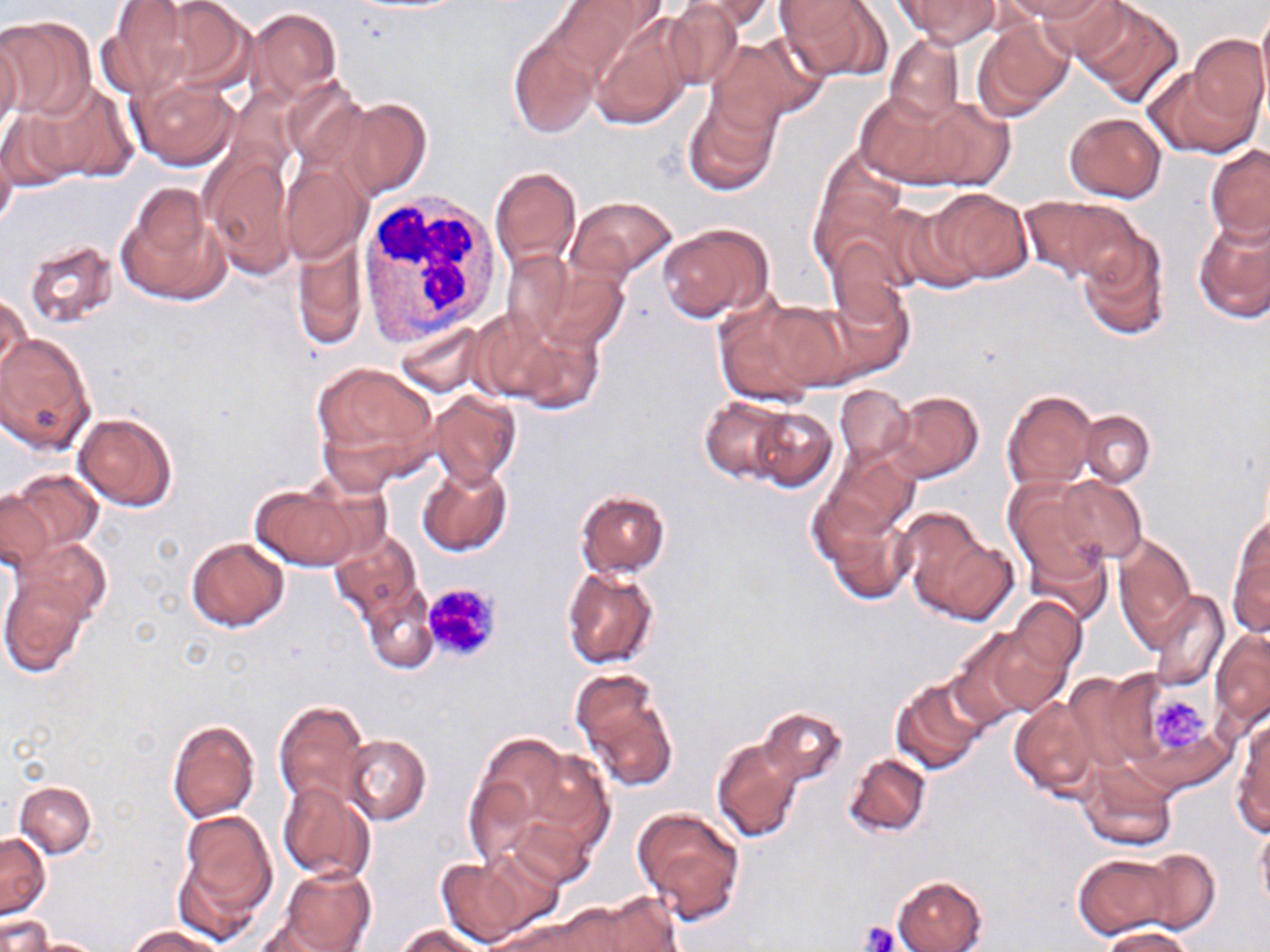
{
  "slide_level_diagnosis": "negative for blood parasites",
  "magnification": "1000x",
  "modality": "optical microscopy",
  "white_blood_cell_locations": "approximate bounding boxes as (x1, y1, x2, y2) in pixels: (358, 192, 506, 345)",
  "platelet_locations": "approximate bounding boxes as (x1, y1, x2, y2) in pixels: (422, 582, 501, 662), (1148, 690, 1212, 755), (860, 922, 900, 952)",
  "field_of_view": "one of a larger specimen",
  "image_size": "1270×952 pixels",
  "preparation": "thin blood film",
  "stain": "May-Grünwald-Giemsa",
  "uninfected_red_blood_cell_locations": "approximate bounding boxes as (x1, y1, x2, y2) in pixels: (154, 0, 259, 94), (550, 0, 658, 79), (680, 0, 777, 32), (776, 0, 888, 82), (894, 0, 1000, 46), (999, 0, 1112, 22), (1038, 0, 1135, 71), (100, 1, 195, 99), (661, 2, 744, 91), (1076, 2, 1183, 106), (1256, 2, 1270, 108), (247, 5, 342, 102), (0, 15, 96, 120), (589, 15, 694, 130), (972, 16, 1073, 121), (508, 30, 599, 137), (0, 31, 22, 143), (709, 33, 826, 130), (1188, 33, 1270, 136), (884, 35, 964, 124), (1143, 62, 1259, 158), (128, 77, 238, 169), (281, 79, 366, 168), (27, 83, 136, 182), (855, 89, 980, 188), (683, 94, 781, 196), (906, 95, 1016, 193), (3, 98, 93, 189), (342, 98, 431, 198), (1064, 113, 1167, 202), (0, 130, 17, 235), (1205, 145, 1270, 245), (200, 150, 296, 274), (811, 155, 905, 273), (281, 160, 371, 263), (489, 166, 582, 269), (118, 184, 228, 306), (925, 187, 1034, 285), (570, 196, 676, 281), (1023, 196, 1141, 285), (880, 202, 984, 294), (1194, 215, 1270, 323), (658, 222, 773, 322), (1077, 231, 1170, 341), (293, 237, 367, 350), (21, 240, 120, 328), (826, 241, 911, 328), (501, 249, 577, 342), (532, 265, 628, 353), (819, 281, 913, 377), (1, 292, 31, 391), (714, 295, 835, 408), (761, 299, 862, 391), (492, 316, 605, 415), (395, 319, 487, 397), (1, 332, 94, 453), (311, 360, 438, 482), (834, 384, 913, 468), (429, 391, 520, 487), (885, 391, 983, 484), (1001, 391, 1097, 490), (699, 397, 795, 484), (747, 405, 839, 493), (1079, 410, 1155, 486), (73, 413, 177, 512), (826, 450, 918, 539), (418, 463, 512, 557), (7, 468, 104, 556), (1055, 475, 1145, 564), (1004, 477, 1114, 592), (249, 484, 360, 570), (575, 490, 670, 578), (814, 490, 917, 604), (0, 491, 55, 574), (902, 512, 1017, 625), (1228, 520, 1270, 638), (330, 531, 424, 622), (1113, 534, 1197, 647), (185, 536, 290, 631), (18, 538, 112, 623), (561, 567, 658, 670), (1, 577, 93, 678), (361, 583, 439, 674), (1150, 590, 1228, 692), (1002, 597, 1086, 690), (949, 628, 1055, 727), (1210, 629, 1269, 728), (1070, 669, 1165, 769), (569, 671, 679, 791), (890, 675, 990, 775), (1008, 696, 1100, 796), (274, 699, 369, 810), (759, 707, 846, 788), (166, 719, 260, 822), (1231, 720, 1270, 834), (340, 734, 430, 824), (712, 738, 804, 843), (470, 740, 610, 875), (845, 753, 932, 837), (1078, 761, 1176, 851), (14, 781, 96, 856), (278, 782, 375, 883), (632, 806, 746, 923), (175, 810, 278, 928), (509, 812, 595, 889), (1254, 820, 1270, 918), (0, 833, 50, 918), (1132, 851, 1219, 932), (436, 852, 549, 948), (1073, 853, 1178, 940), (278, 865, 376, 952), (893, 876, 987, 952), (569, 895, 681, 951), (495, 911, 620, 952), (2, 914, 50, 952), (255, 916, 350, 952), (394, 923, 487, 952), (127, 925, 223, 952), (1100, 926, 1197, 952), (26, 937, 105, 951)"
}